Report the malaria status of this cell.
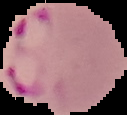

It is parasitized.

image_size: 127×115 pixels
preparation: thin blood smear
image_type: segmented cell region with the area outside set to black